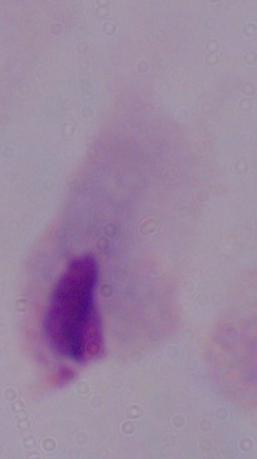
Summary:
  - Modality: photomicrograph
  - Identification: trichomonad
  - Magnification: 1000x